Locate every malaria parasite and every leukocyte.
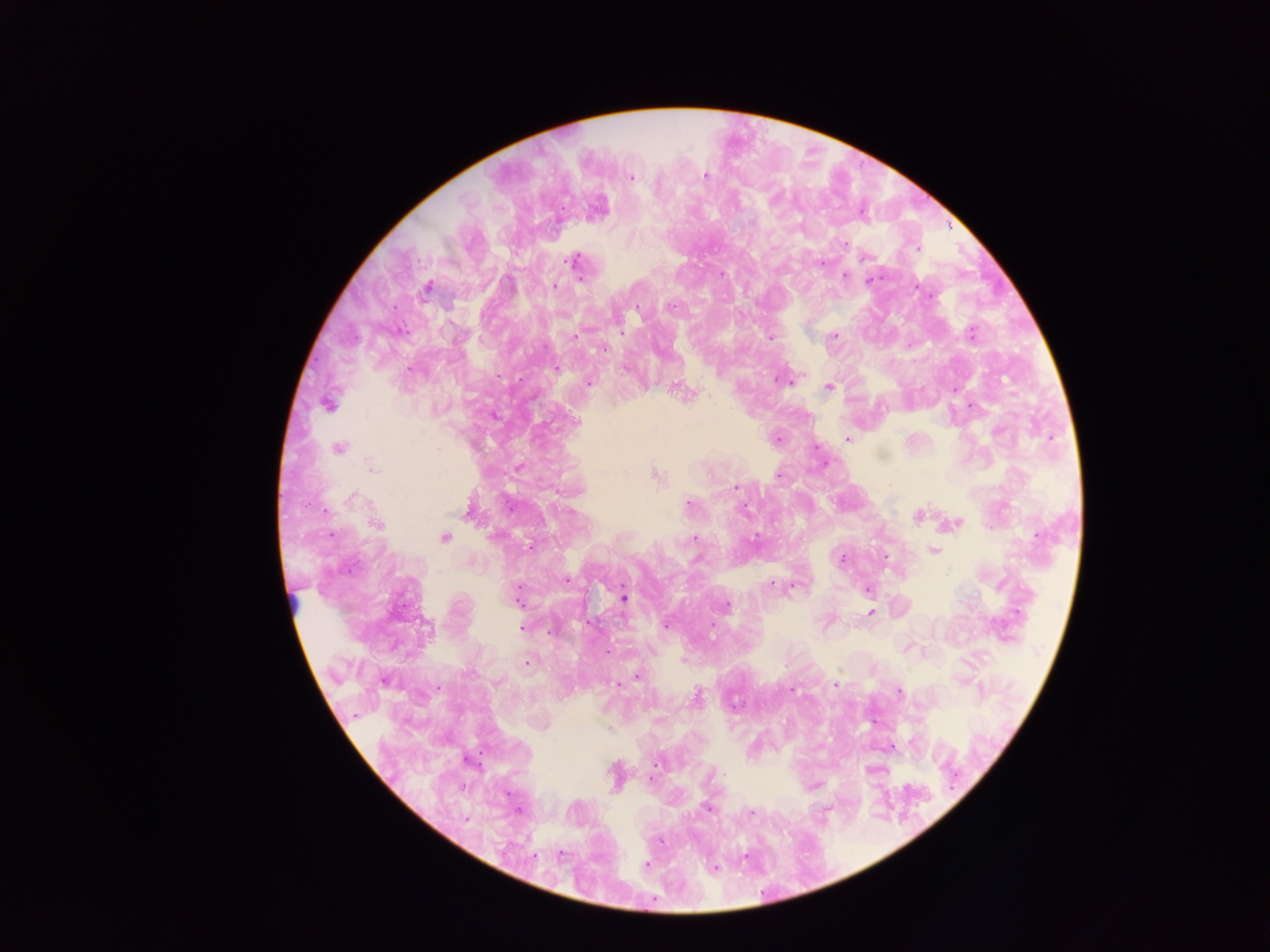
Approximate centers as [x, y] in pixels.
Malaria parasites: [631, 176], [705, 176], [844, 244], [917, 248], [866, 257], [573, 260], [821, 263], [722, 274], [845, 276], [871, 279], [554, 286], [917, 287], [426, 288], [671, 306], [637, 309], [971, 333], [834, 336], [771, 337], [605, 349], [556, 369], [802, 376], [778, 380], [589, 382], [828, 388], [680, 390], [327, 405], [575, 421], [847, 439], [339, 447], [519, 466], [372, 467], [656, 476], [737, 487], [353, 498], [689, 505], [744, 508], [469, 511], [918, 516], [377, 524], [956, 524], [445, 538], [694, 539], [530, 547], [933, 550], [886, 558], [842, 560], [567, 580], [772, 585], [867, 589], [517, 595], [624, 597], [727, 606], [871, 612], [666, 626], [522, 627], [712, 627], [428, 628], [608, 652], [527, 664], [637, 675], [618, 684], [836, 684], [792, 690], [899, 691], [696, 697], [657, 763], [707, 809], [750, 812], [466, 820], [659, 840], [560, 855], [646, 864], [714, 868].
Leukocytes: [295, 601].

Summary:
  - Capture: mobile-phone photograph through a microscope
  - Preparation: thick blood film
  - Field of view: single
  - Country: Ghana
  - Image size: 1270×952 pixels